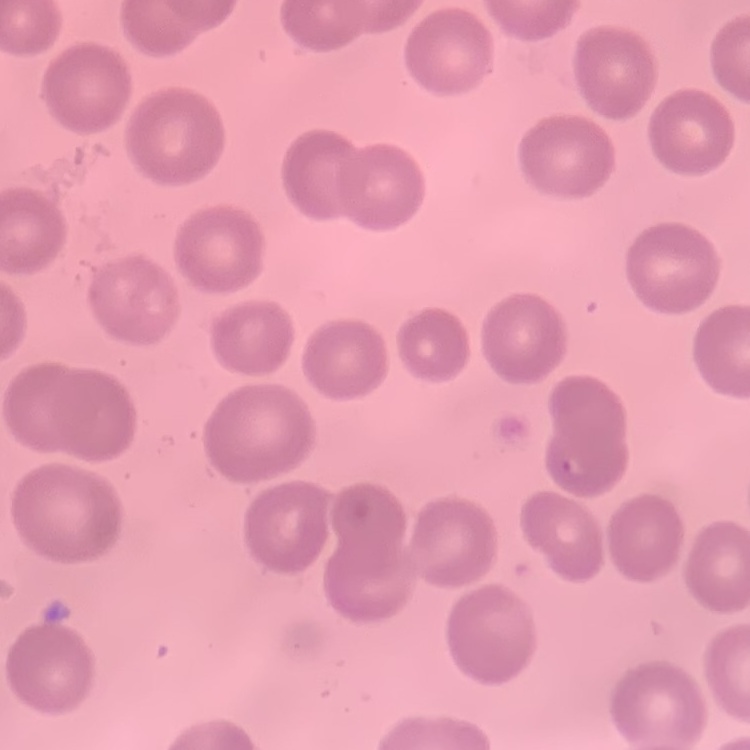

Summary:
  - Erythrocyte morphology: no rouleaux formation
  - Preparation: thin blood smear
  - Stain: Field's or Giemsa
  - Image type: one tile cut from a larger photomicrograph